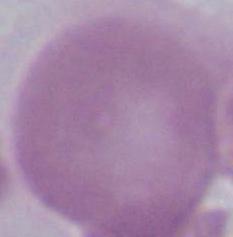

Captured at 1000x magnification. An erythrocyte is seen. Micrograph.